Mark where leukocytes are.
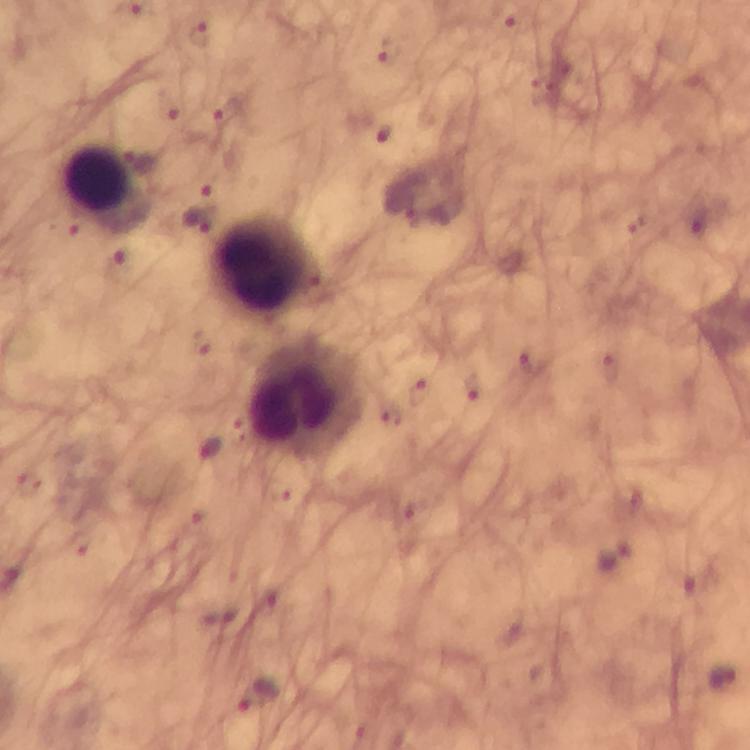

Approximate centers as (x, y) in pixels.
Leukocytes: (99, 180), (262, 263), (306, 399).

Malaria parasite locations: (200, 36), (387, 52), (169, 103), (226, 109), (383, 135), (206, 184), (199, 219), (471, 386), (419, 395), (615, 557), (722, 679), (256, 696). Image is 750×750 pixels. Photographed with a smartphone mounted on the microscope. Thick blood film. 100x magnification. Giemsa stain. Immersion oil applied. Cropped region of a single field of view. From a diagnostic examination for malaria.